Classify this cell by malaria status.
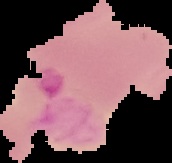
It is parasitized.

image_size: 172×163 pixels
image_type: cell region segmented out of the field of view; surrounding area masked to black
preparation: thin blood smear